Give the position of every Plasmodium parasite visible.
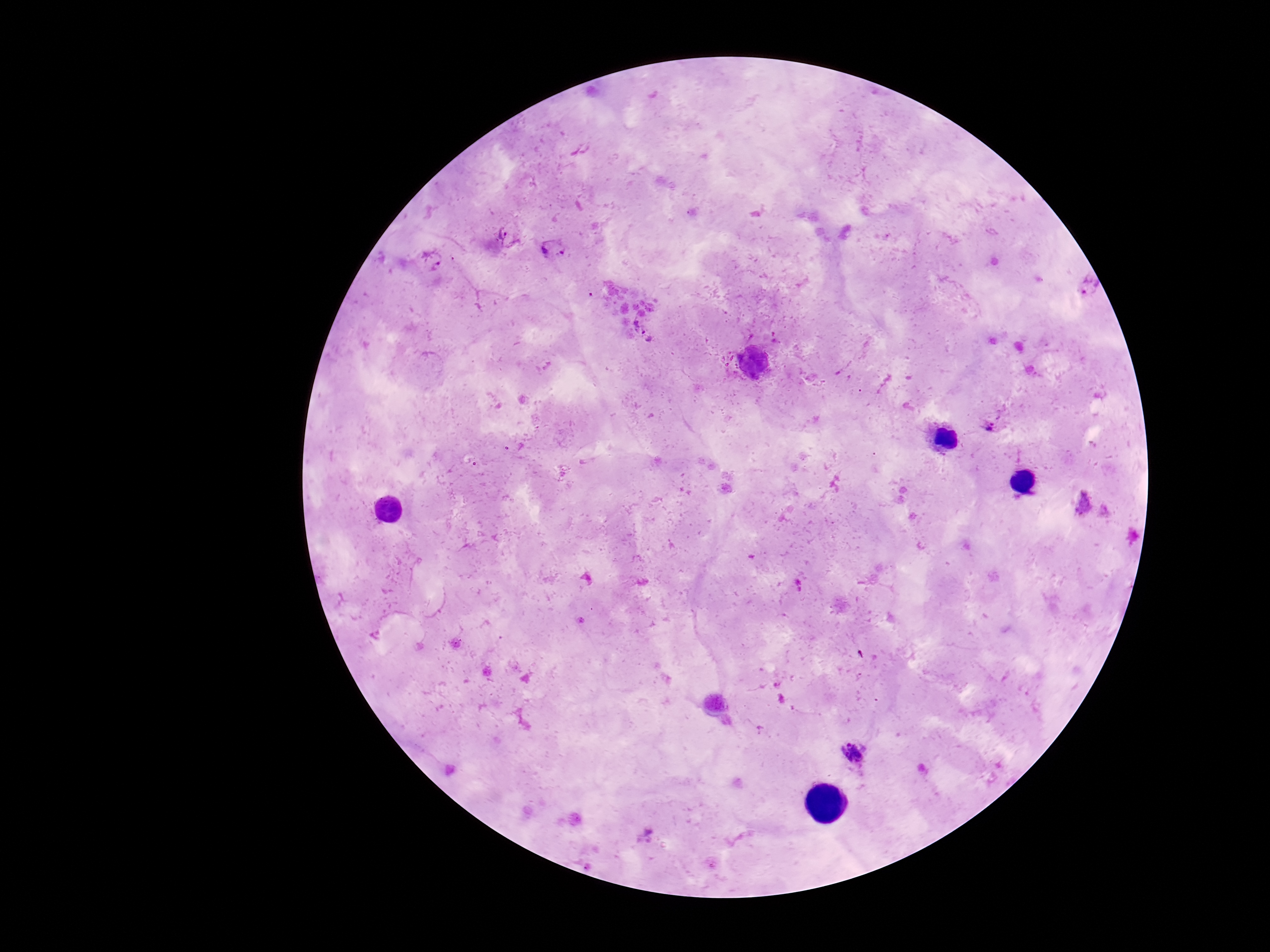
Approximate centers as [x, y] in pixels.
Plasmodium parasites: [502, 234], [552, 249], [434, 259], [1089, 284], [645, 335], [990, 425], [1084, 503], [854, 754], [651, 835].

Summary:
  - Stain: Giemsa
  - Field of view: single
  - Patient malaria status: infected
  - Capture: smartphone camera through the microscope eyepiece
  - Image size: 1270×952 pixels
  - Magnification: 100x
  - Preparation: thick peripheral-blood smear